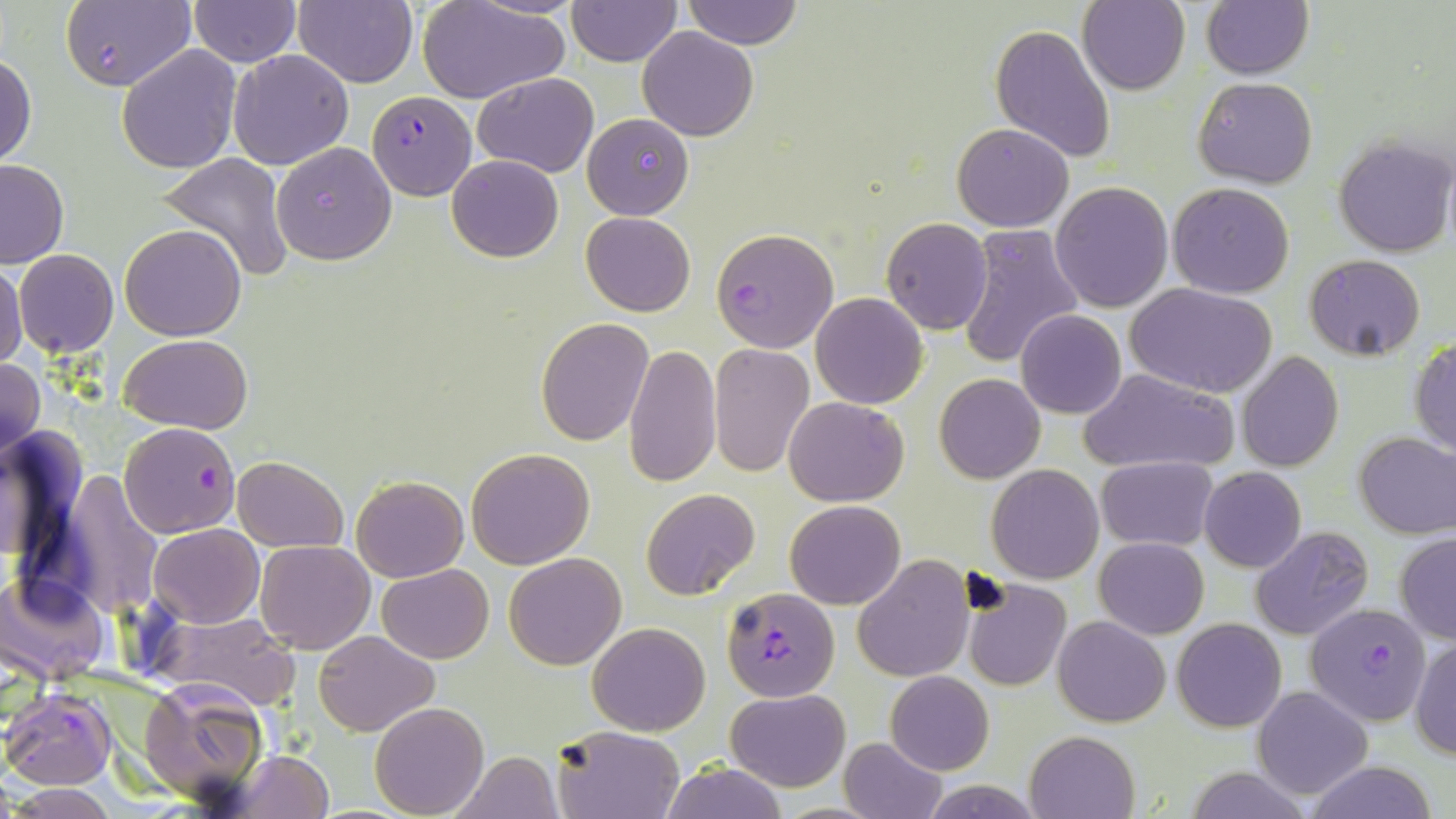
Approximate bounding boxes as (x1, y1, x2, y2) in pixels. Uninfected red blood cell locations: (62, 0, 196, 93), (293, 0, 418, 87), (566, 0, 682, 67), (683, 0, 803, 49), (1079, 1, 1190, 96), (189, 2, 300, 65), (1200, 2, 1313, 79), (418, 3, 567, 104), (989, 23, 1116, 164), (638, 27, 759, 142), (116, 44, 241, 174), (228, 48, 355, 171), (1, 51, 38, 166), (472, 71, 599, 176), (1192, 76, 1318, 188), (582, 113, 694, 219), (952, 123, 1075, 232), (1333, 135, 1454, 258), (272, 141, 397, 266), (157, 153, 294, 282), (446, 154, 564, 262), (0, 159, 69, 267), (1050, 182, 1173, 313), (1168, 183, 1295, 298), (581, 211, 694, 316), (881, 217, 994, 334), (120, 224, 245, 340), (955, 225, 1085, 369), (15, 250, 119, 357), (1305, 255, 1427, 360), (0, 258, 27, 373), (1126, 282, 1278, 398), (811, 293, 928, 409), (1015, 310, 1126, 419), (535, 317, 653, 444), (121, 334, 253, 435), (1409, 335, 1456, 458), (624, 343, 721, 489), (709, 343, 813, 477), (1237, 351, 1343, 473), (0, 358, 45, 464), (1079, 367, 1237, 475), (935, 373, 1044, 484), (784, 396, 908, 506), (1354, 430, 1456, 539), (466, 447, 595, 569), (232, 455, 347, 552), (1096, 456, 1218, 552), (987, 464, 1103, 584), (1199, 467, 1306, 572), (53, 472, 167, 617), (351, 475, 468, 582), (640, 487, 761, 600), (785, 500, 905, 609), (149, 523, 263, 627), (1251, 527, 1374, 642), (1394, 534, 1456, 644), (1094, 537, 1208, 638), (255, 540, 375, 654), (504, 552, 627, 670), (853, 554, 974, 682), (376, 564, 494, 663), (2, 573, 108, 682), (961, 579, 1070, 692), (155, 614, 298, 710), (1053, 614, 1171, 726), (1172, 618, 1286, 731), (588, 622, 711, 735), (312, 630, 438, 736), (1409, 635, 1456, 760), (886, 670, 994, 775), (135, 680, 272, 809), (1253, 685, 1374, 800), (724, 689, 849, 791), (371, 702, 490, 817), (555, 728, 684, 818), (1025, 730, 1139, 819), (840, 737, 947, 819), (230, 750, 332, 818), (449, 751, 564, 818), (1304, 761, 1437, 819), (658, 764, 788, 818), (1185, 766, 1313, 819), (919, 778, 1041, 817), (7, 785, 119, 818). Plasmodium falciparum-infected red blood cell locations: (367, 89, 475, 199), (713, 226, 837, 352), (118, 421, 240, 537), (722, 585, 839, 700), (1306, 608, 1433, 729), (3, 688, 115, 788). Slide-level diagnosis: Plasmodium falciparum. Image is 1456×819 pixels. Thin blood film. One field of a larger specimen. May-Grünwald-Giemsa-stained preparation. Optical microscopy. Captured at 1000x magnification.